Classify this cell by malaria status.
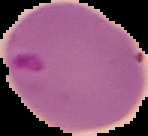
It is parasitized.

Image is 148×136 pixels. The area outside the segmented cell region is set to black. From a thin blood film.